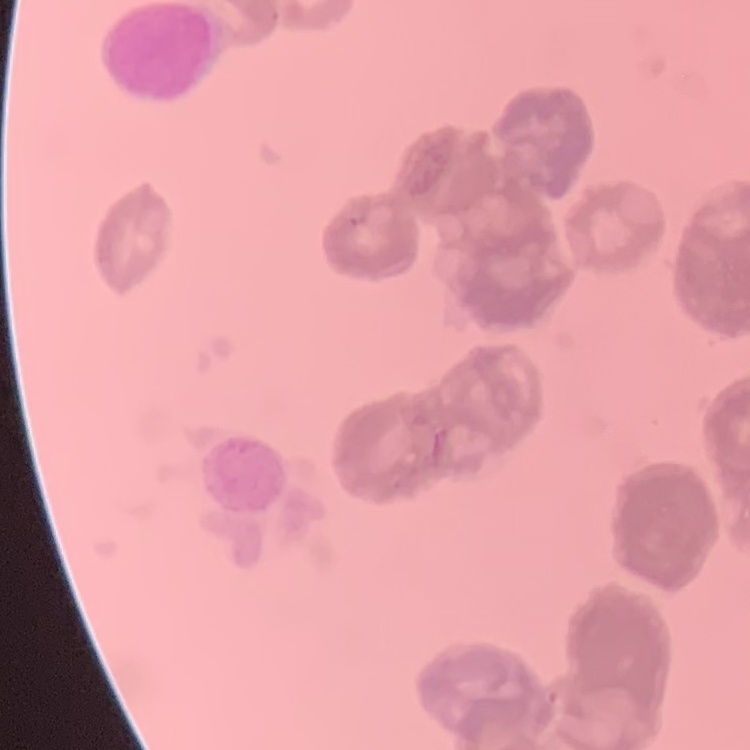

{
  "red_blood_cell_morphology": "rouleaux formation",
  "stain": "Field's or Giemsa",
  "image_type": "one tile cut from a larger photomicrograph",
  "preparation": "thin peripheral smear"
}